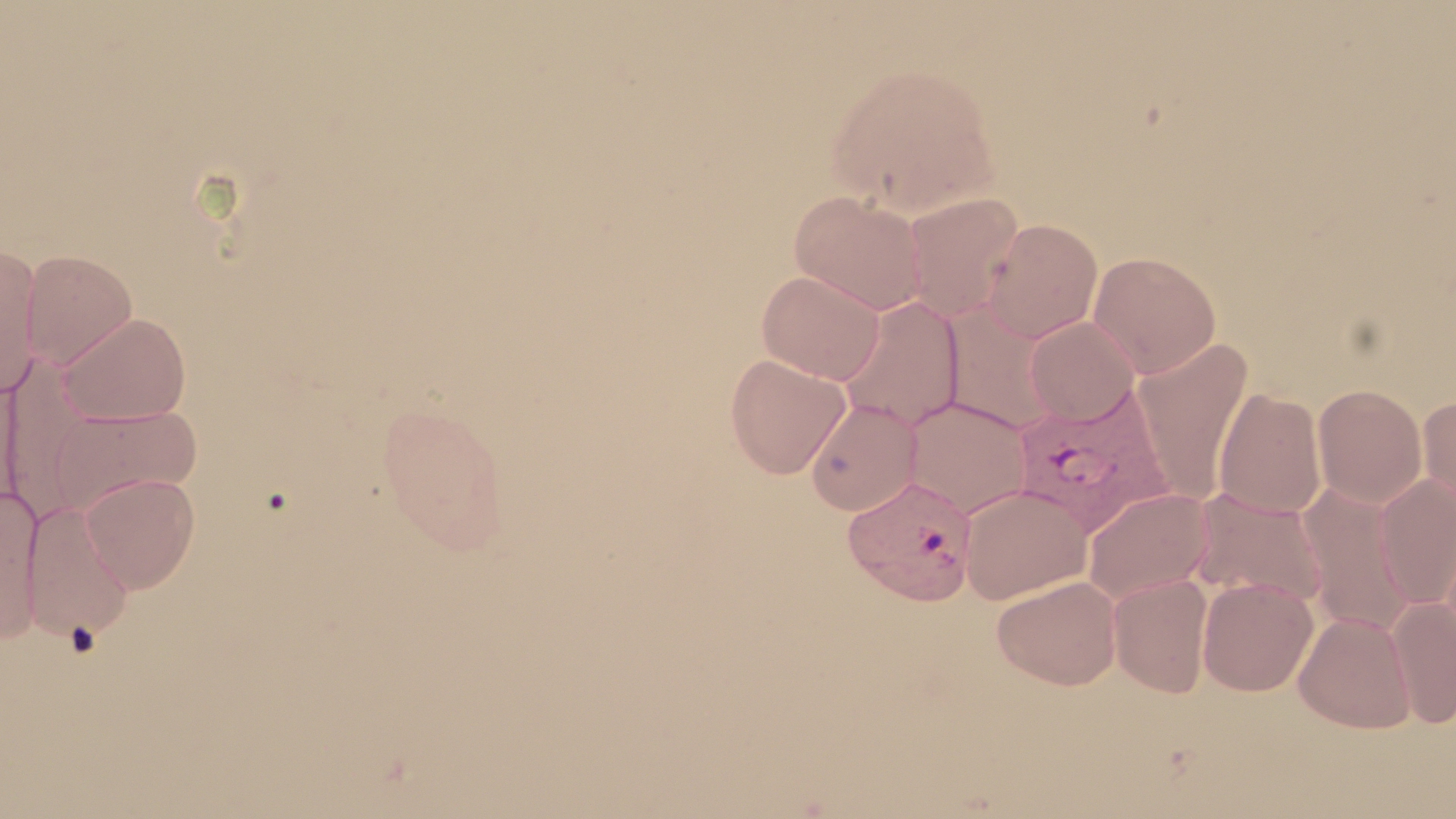

{
  "plasmodium_vivax_infected_red_blood_cell_locations": "approximate bounding boxes as (x1,y1)-(x2,y2) corner pairs in pixels: (1011,387)-(1172,536), (843,476)-(977,606)",
  "slide_level_diagnosis": "Plasmodium vivax",
  "image_size": "1456×819 pixels",
  "stain": "May-Grünwald-Giemsa",
  "field_of_view": "one of a larger specimen",
  "preparation": "thin blood smear",
  "modality": "light microscopy",
  "uninfected_red_blood_cell_locations": "approximate bounding boxes as (x1,y1)-(x2,y2) corner pairs in pixels: (825,60)-(1000,219), (788,190)-(928,315), (903,193)-(1026,323), (982,219)-(1103,342), (0,244)-(41,397), (21,250)-(138,369), (1088,251)-(1221,378), (757,270)-(886,384), (837,295)-(966,432), (941,302)-(1063,436), (59,312)-(192,426), (1025,316)-(1140,424), (1133,338)-(1253,506), (2,354)-(102,522), (725,354)-(851,479), (0,367)-(22,515), (1313,384)-(1427,508), (1214,388)-(1326,519), (1418,394)-(1456,514), (903,397)-(1034,518), (805,398)-(923,516), (376,402)-(513,551), (47,403)-(202,517), (81,473)-(200,593), (1375,473)-(1456,610), (1298,482)-(1416,635), (0,485)-(44,641), (958,486)-(1092,605), (1082,487)-(1215,605), (1188,487)-(1328,609), (22,500)-(134,643), (1108,574)-(1213,697), (992,575)-(1122,691), (1197,577)-(1319,697), (1387,598)-(1456,728), (1294,610)-(1416,733)",
  "magnification": "1000x"
}